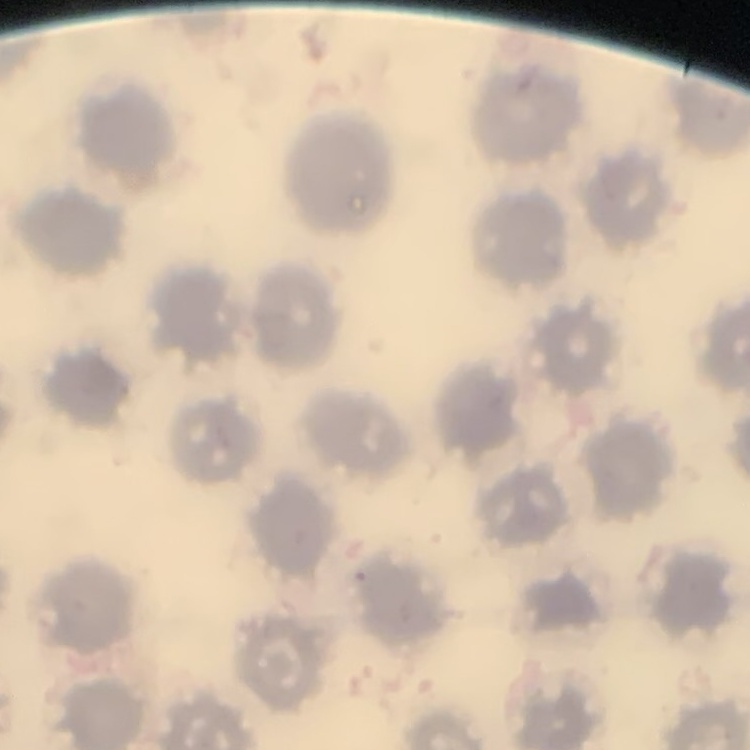
Summary:
  - Red blood cell morphology: no rouleaux formation
  - Image type: square crop of a larger photomicrograph
  - Stain: Field's or Giemsa
  - Preparation: thin blood smear